Report the malaria status of this cell.
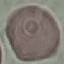
It is uninfected.

stain = Giemsa
preparation = thin blood film
capture = smartphone through the microscope eyepiece
image type = cell patch, automatically extracted from a larger field of view and resized to 64 × 64 pixels